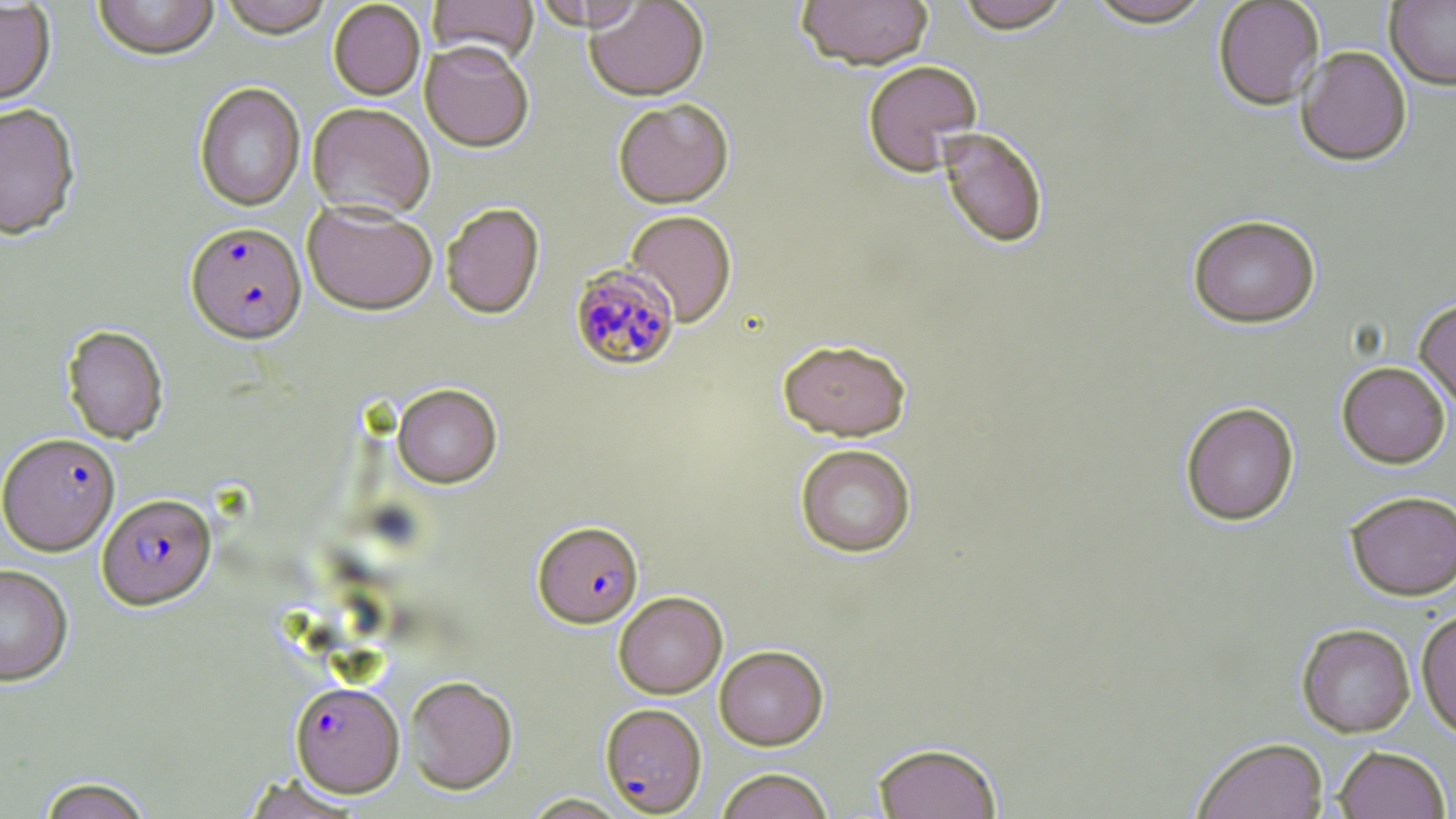
slide-level diagnosis = Plasmodium falciparum
modality = light microscopy
field of view = single
Plasmodium falciparum-infected red blood cell locations = approximate bounding boxes as (x1,y1)-(x2,y2) corner pairs in pixels: (186,221)-(306,344), (568,263)-(680,371), (1,434)-(120,555), (98,493)-(216,610), (533,520)-(644,628), (290,681)-(404,796), (603,703)-(709,816)
stain = May-Grünwald-Giemsa
image size = 1456×819 pixels
uninfected red blood cell locations = approximate bounding boxes as (x1,y1)-(x2,y2) corner pairs in pixels: (92,0)-(220,62), (218,0)-(333,39), (427,0)-(538,65), (796,0)-(933,72), (955,0)-(1074,35), (1084,0)-(1216,30), (1213,0)-(1324,110), (0,1)-(56,108), (328,1)-(426,100), (530,1)-(646,31), (585,1)-(709,101), (1385,1)-(1456,89), (420,41)-(535,152), (1296,46)-(1412,166), (862,60)-(983,176), (194,83)-(306,211), (613,98)-(734,208), (307,102)-(435,219), (0,105)-(81,240), (937,128)-(1049,249), (302,199)-(438,314), (441,203)-(545,319), (624,210)-(737,326), (1187,215)-(1321,328), (1414,299)-(1456,412), (61,325)-(169,445), (777,338)-(912,441), (1337,361)-(1451,468), (393,384)-(502,488), (1180,402)-(1299,526), (795,444)-(917,557), (1344,490)-(1456,600), (0,563)-(73,686), (614,591)-(727,698), (1416,610)-(1456,738), (1297,623)-(1415,737), (715,645)-(828,749), (404,675)-(518,794), (1191,737)-(1329,819), (872,742)-(1003,819), (1333,745)-(1451,819), (716,769)-(834,819), (34,776)-(154,819), (521,793)-(631,818)
magnification = 1000x
preparation = thin blood film